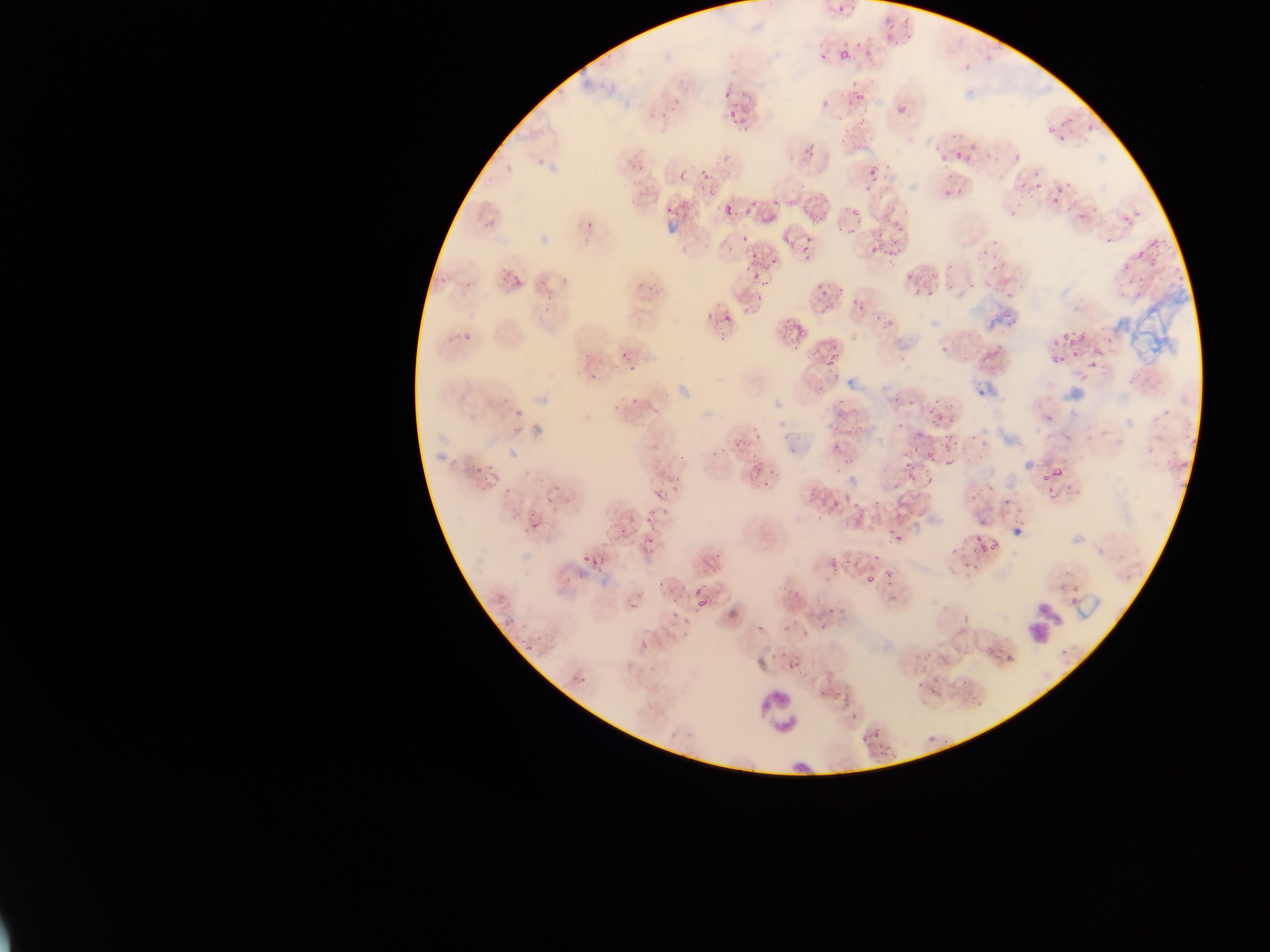

Approximate bounding boxes as left top right bottom in pixels. Malaria parasite locations: 836 43 855 61; 854 89 867 102; 723 90 731 99; 896 106 904 114; 725 109 744 124; 1052 119 1082 144; 951 144 969 160; 866 160 883 181; 699 169 709 179; 1020 170 1040 195; 678 172 687 181; 1049 185 1073 207; 707 187 716 196; 767 190 791 211; 684 202 706 223; 846 203 857 217; 719 205 736 217; 666 206 674 215; 808 210 824 230; 1119 211 1132 223; 741 231 749 240; 866 233 895 253; 1130 234 1163 264; 780 236 796 256; 797 238 816 263; 747 247 764 269; 904 270 916 281; 748 274 759 285; 508 275 524 288; 821 280 839 296; 911 281 933 298; 996 307 1013 327; 719 314 733 323; 789 318 806 337; 1061 329 1078 348; 466 331 480 344; 821 346 844 371; 1069 348 1084 359; 1043 351 1061 364; 1086 359 1096 374; 588 373 598 382; 813 382 829 395; 935 409 950 426; 849 422 868 437; 738 427 768 445; 944 429 953 460; 923 432 933 441; 925 447 941 461; 466 458 485 482; 749 464 769 487; 901 464 913 476; 1039 467 1064 486; 808 479 822 504; 999 490 1015 513; 643 512 658 524; 530 515 542 531; 892 525 913 540; 968 534 992 555; 825 546 848 571; 581 551 590 564; 883 568 894 577; 862 572 876 585; 688 573 709 614; 830 694 853 709; 861 726 883 744. Leukocyte locations: 1022 603 1061 647; 756 689 804 733. Image is 1270×952 pixels. Mobile-phone photograph taken through the microscope. Thin blood smear. Sample from Ghana. Single field of view.